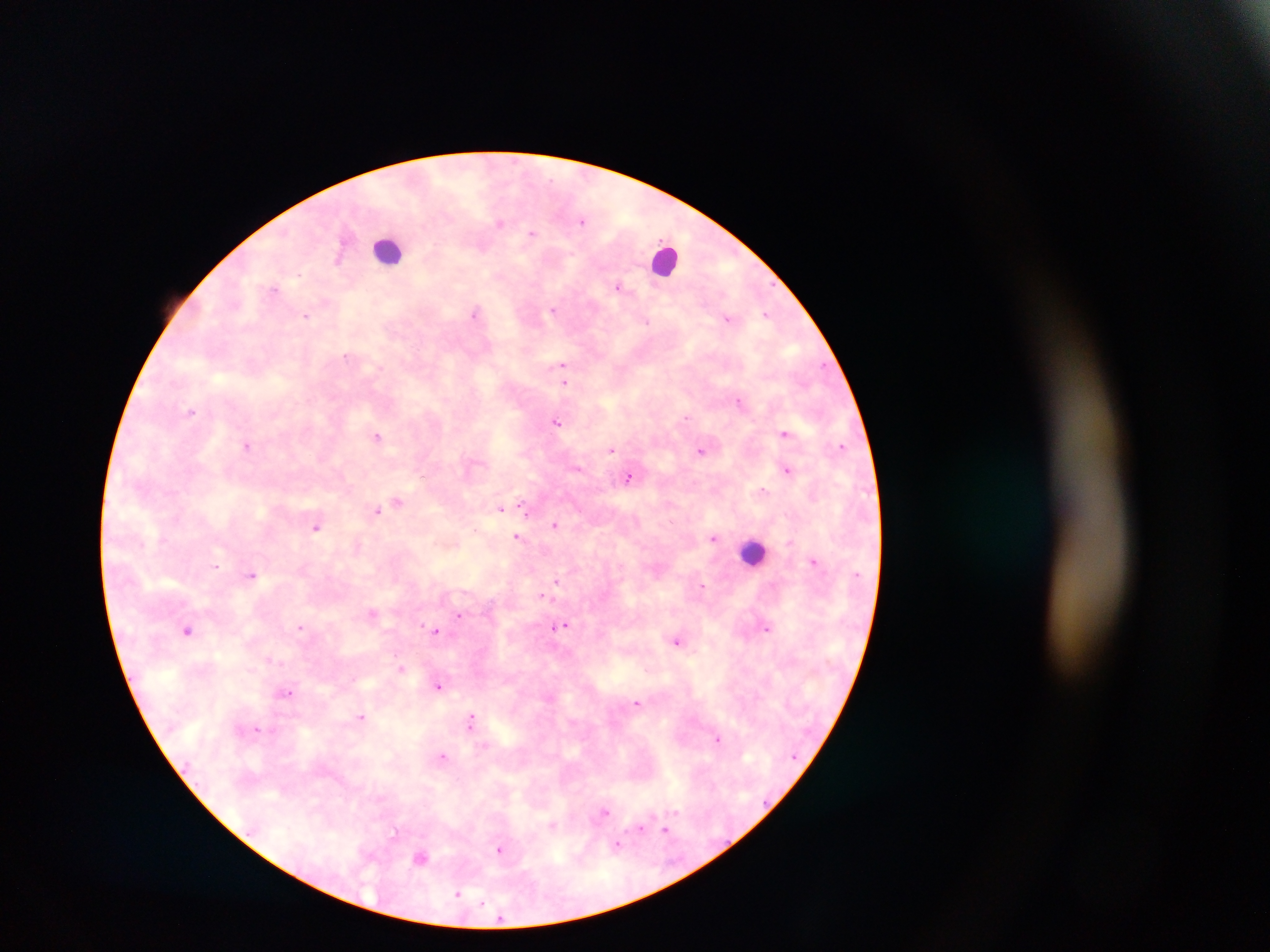

Approximate centers as [x, y] in pixels.
Summary:
  - Plasmodium parasite locations: [582, 221], [500, 223], [532, 233], [482, 246], [339, 258], [618, 286], [274, 289], [554, 309], [475, 313], [766, 314], [306, 316], [727, 318], [647, 322], [346, 356], [562, 365], [823, 366], [564, 382], [738, 401], [191, 411], [686, 417], [556, 422], [785, 433], [377, 436], [247, 445], [841, 446], [611, 450], [701, 450], [787, 470], [423, 475], [629, 477], [763, 490], [397, 501], [523, 506], [501, 508], [377, 510], [526, 511], [316, 526], [557, 527], [475, 530], [517, 537], [713, 538], [814, 561], [216, 566], [252, 575], [556, 581], [703, 586], [541, 595], [372, 613], [459, 615], [562, 625], [300, 628], [767, 628], [188, 630], [436, 632], [677, 640], [269, 660], [401, 667], [438, 686], [287, 693], [637, 702], [362, 716], [471, 721], [257, 729], [717, 738], [443, 757], [676, 811], [604, 813], [553, 826], [640, 828], [666, 830], [395, 831], [617, 844], [499, 850], [420, 857], [458, 894], [483, 903]
  - Leukocyte locations: [388, 250], [666, 259], [754, 552]
  - Image size: 1270×952 pixels
  - Field of view: single
  - Preparation: thick blood smear
  - Capture: mobile-phone photograph through a microscope
  - Country: Ghana